Classify this cell by malaria status.
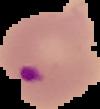

Parasitized.

From a thin blood film. Image is 100×109 pixels. Segmented cell region on a black background.